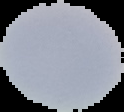
{
  "preparation": "thin blood smear",
  "image_type": "segmented cell region with the area outside set to black",
  "image_size": "124×112 pixels",
  "result": "no malaria parasites detected"
}